Locate every malaria parasite.
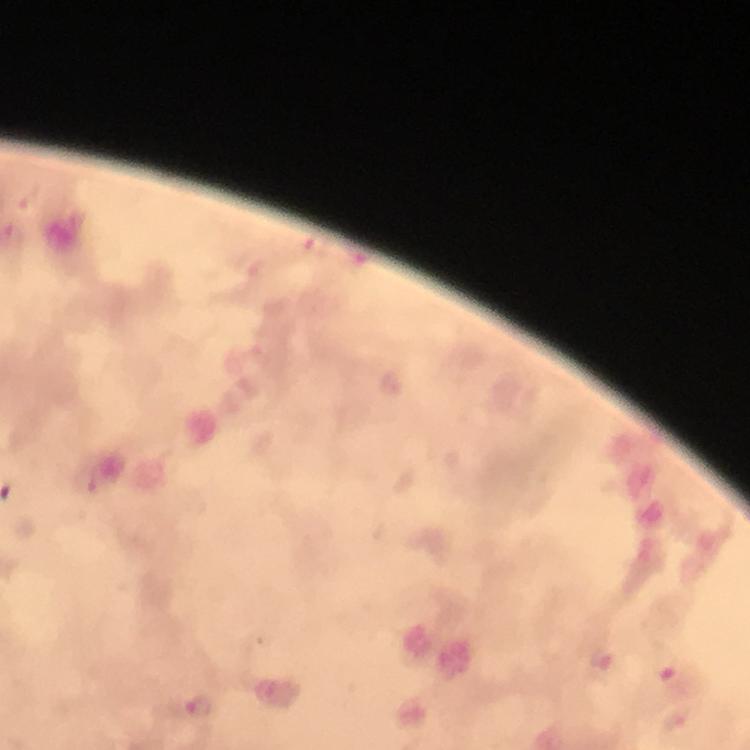
Approximate centers as (x, y) in pixels.
Malaria parasites: (31, 197), (12, 237), (311, 250), (358, 263), (253, 264), (198, 706).

{
  "immersion_oil": "applied",
  "stain": "Giemsa",
  "magnification": "100x",
  "image_size": "750×750 pixels",
  "capture": "smartphone mounted on the microscope",
  "context": "from a malaria diagnostic workup",
  "preparation": "thick blood film",
  "cropped_from": "one field of view"
}